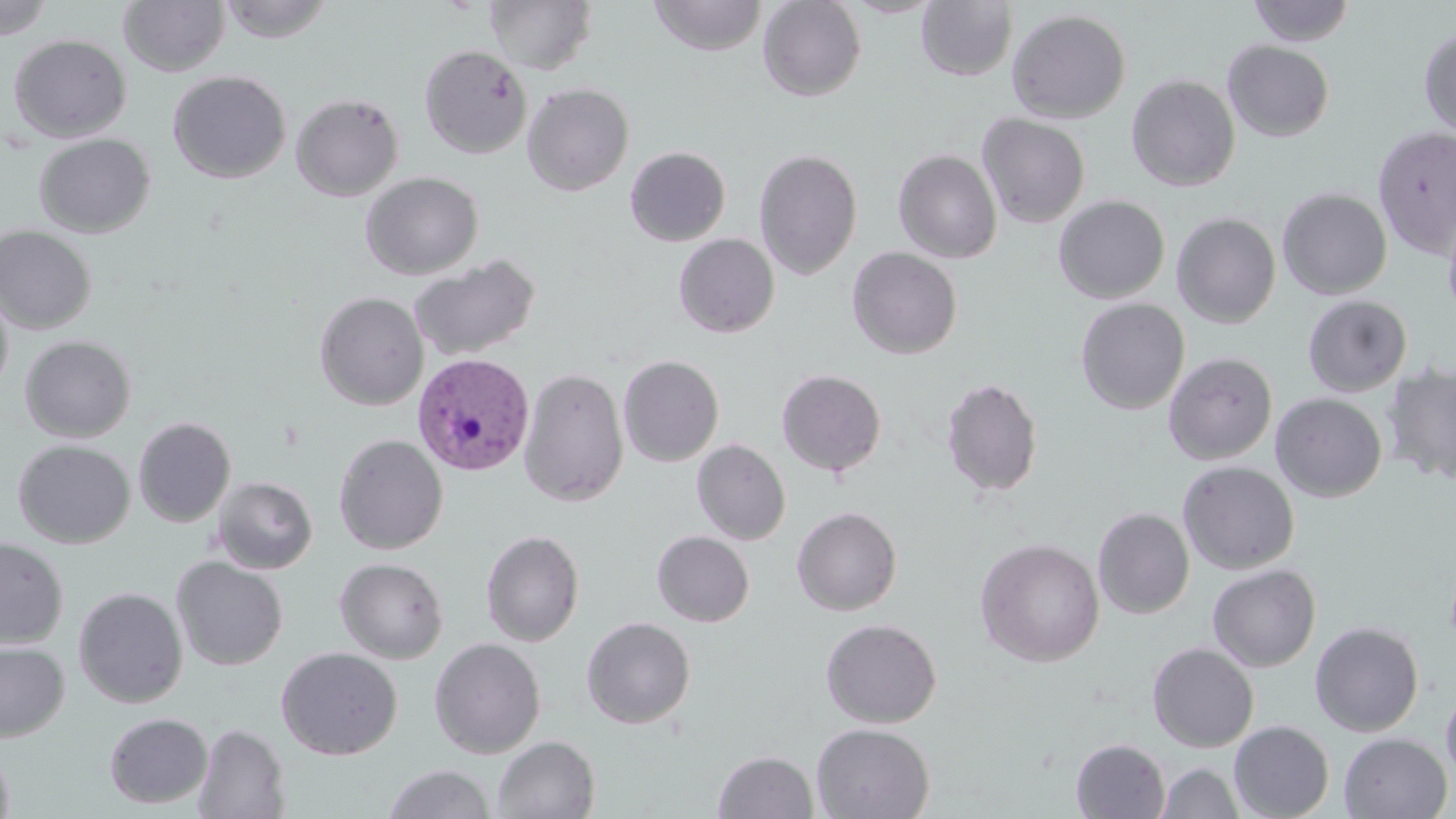
plasmodium_vivax_infected_red_blood_cell_locations: 'approximate bounding boxes as named x1/y1/x2/y2 corners in pixels: (x1=407, y1=355, x2=538, y2=478)'
slide_level_diagnosis: Plasmodium vivax
magnification: 1000x
field_of_view: one of a larger specimen
stain: May-Grünwald-Giemsa
image_size: 1456×819 pixels
modality: optical microscopy
uninfected_red_blood_cell_locations: 'approximate bounding boxes as named x1/y1/x2/y2 corners in pixels: (x1=218, y1=0, x2=333, y2=43), (x1=485, y1=0, x2=597, y2=75), (x1=649, y1=0, x2=767, y2=56), (x1=757, y1=0, x2=866, y2=101), (x1=1247, y1=0, x2=1356, y2=46), (x1=0, y1=1, x2=54, y2=40), (x1=119, y1=1, x2=229, y2=77), (x1=917, y1=1, x2=1017, y2=81), (x1=1007, y1=8, x2=1131, y2=123), (x1=1419, y1=26, x2=1456, y2=138), (x1=8, y1=34, x2=132, y2=143), (x1=1222, y1=40, x2=1334, y2=142), (x1=419, y1=44, x2=532, y2=159), (x1=168, y1=70, x2=291, y2=184), (x1=1126, y1=73, x2=1241, y2=192), (x1=521, y1=83, x2=634, y2=196), (x1=290, y1=92, x2=404, y2=202), (x1=977, y1=113, x2=1090, y2=228), (x1=1373, y1=125, x2=1456, y2=258), (x1=33, y1=133, x2=155, y2=238), (x1=625, y1=146, x2=731, y2=246), (x1=754, y1=147, x2=863, y2=280), (x1=893, y1=149, x2=1002, y2=264), (x1=360, y1=171, x2=484, y2=280), (x1=1277, y1=188, x2=1392, y2=300), (x1=1053, y1=195, x2=1170, y2=303), (x1=1442, y1=210, x2=1456, y2=325), (x1=1171, y1=212, x2=1281, y2=328), (x1=0, y1=225, x2=97, y2=335), (x1=673, y1=234, x2=780, y2=338), (x1=846, y1=247, x2=963, y2=359), (x1=409, y1=254, x2=541, y2=362), (x1=0, y1=282, x2=14, y2=400), (x1=314, y1=291, x2=428, y2=410), (x1=1303, y1=295, x2=1412, y2=397), (x1=1075, y1=297, x2=1190, y2=415), (x1=1123, y1=330, x2=1243, y2=451), (x1=20, y1=335, x2=137, y2=442), (x1=1163, y1=352, x2=1277, y2=465), (x1=618, y1=355, x2=724, y2=466), (x1=1381, y1=362, x2=1456, y2=485), (x1=518, y1=367, x2=629, y2=506), (x1=776, y1=369, x2=887, y2=477), (x1=941, y1=377, x2=1044, y2=499), (x1=1270, y1=393, x2=1387, y2=502), (x1=133, y1=417, x2=236, y2=527), (x1=333, y1=434, x2=448, y2=554), (x1=12, y1=439, x2=135, y2=548), (x1=692, y1=439, x2=791, y2=545), (x1=1178, y1=461, x2=1299, y2=574), (x1=213, y1=477, x2=318, y2=574), (x1=792, y1=506, x2=902, y2=616), (x1=1093, y1=507, x2=1194, y2=619), (x1=480, y1=529, x2=584, y2=647), (x1=652, y1=531, x2=754, y2=626), (x1=0, y1=536, x2=68, y2=649), (x1=976, y1=538, x2=1105, y2=667), (x1=172, y1=557, x2=288, y2=670), (x1=335, y1=557, x2=448, y2=664), (x1=1207, y1=564, x2=1321, y2=672), (x1=73, y1=587, x2=188, y2=708), (x1=581, y1=616, x2=696, y2=729), (x1=820, y1=618, x2=942, y2=728), (x1=1310, y1=621, x2=1424, y2=737), (x1=428, y1=637, x2=547, y2=758), (x1=0, y1=641, x2=69, y2=743), (x1=1147, y1=642, x2=1259, y2=752), (x1=276, y1=647, x2=403, y2=760), (x1=1441, y1=681, x2=1456, y2=787), (x1=104, y1=712, x2=213, y2=809), (x1=1229, y1=720, x2=1334, y2=819), (x1=193, y1=723, x2=290, y2=818), (x1=811, y1=723, x2=935, y2=819), (x1=1338, y1=732, x2=1453, y2=818), (x1=493, y1=736, x2=600, y2=818), (x1=1072, y1=739, x2=1170, y2=818), (x1=0, y1=743, x2=15, y2=819), (x1=713, y1=750, x2=818, y2=818), (x1=1156, y1=763, x2=1244, y2=819), (x1=382, y1=764, x2=496, y2=818)'
preparation: thin blood film